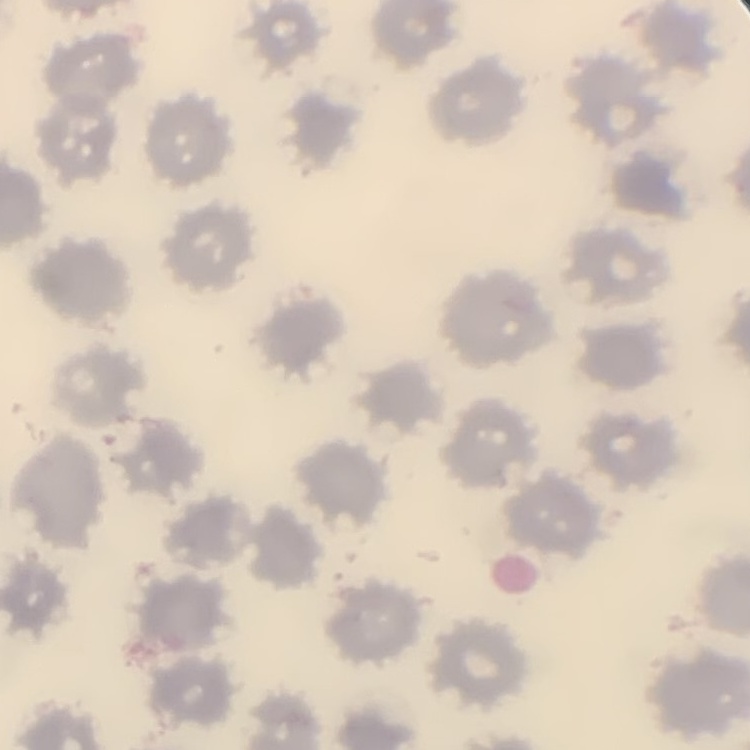

erythrocyte morphology = no rouleaux formation
preparation = thin blood film
stain = Field's or Giemsa
image type = one tile cut from a larger photomicrograph